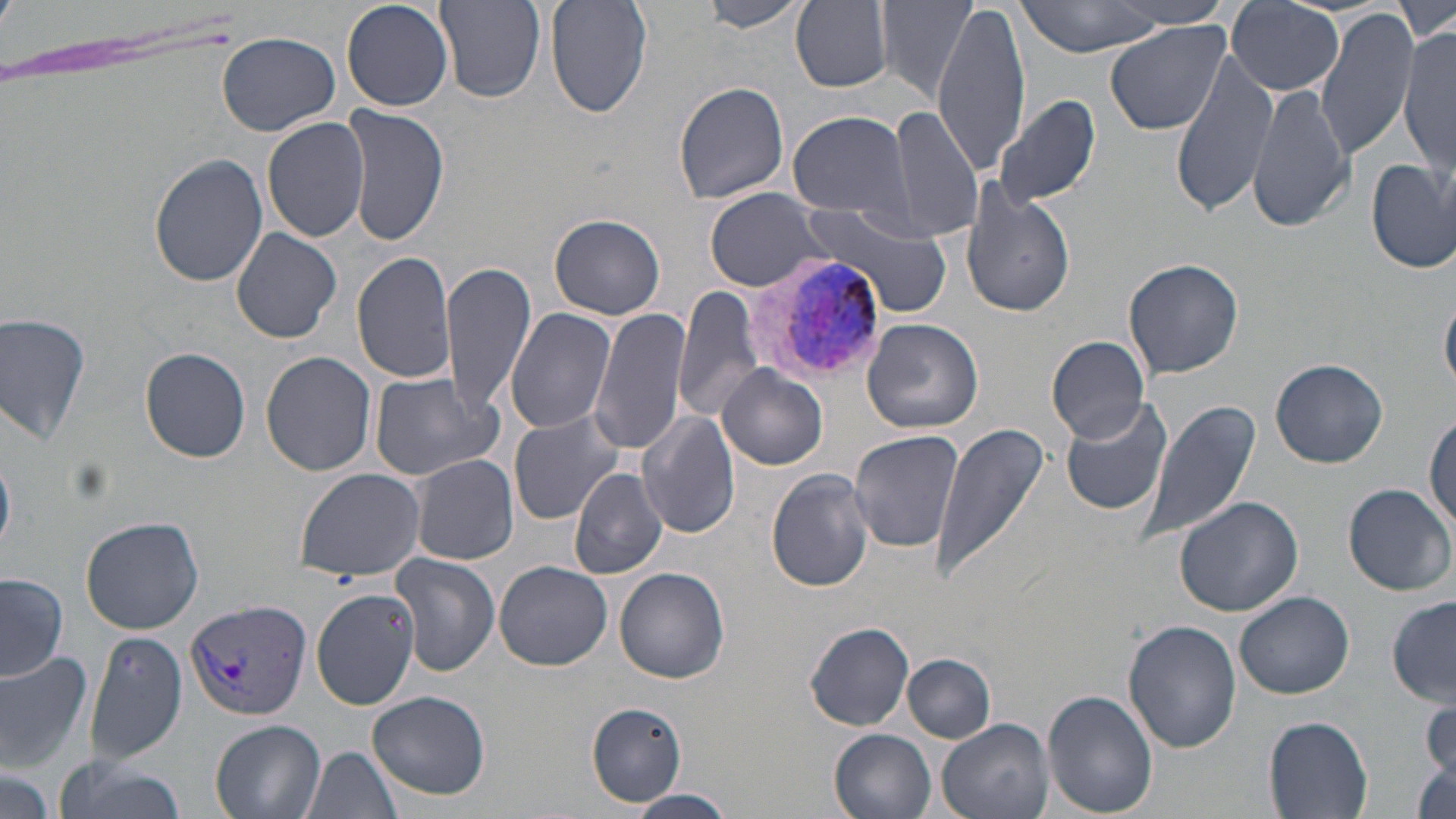

slide-level diagnosis = Plasmodium vivax
preparation = thin blood smear
field of view = one of a larger specimen
Plasmodium vivax-infected red blood cell locations = approximate bounding boxes as (x1,y1)-(x2,y2) corner pairs in pixels: (740,248)-(886,384), (183,597)-(311,723)
modality = light microscopy
magnification = 1000x
image size = 1456×819 pixels
uninfected red blood cell locations = approximate bounding boxes as (x1,y1)-(x2,y2) corner pairs in pixels: (342,0)-(454,112), (546,0)-(652,121), (875,0)-(978,101), (1012,0)-(1170,57), (1395,0)-(1455,44), (435,1)-(546,103), (701,1)-(809,33), (791,1)-(893,91), (1110,1)-(1234,30), (1224,2)-(1346,95), (931,5)-(1029,173), (1315,8)-(1417,162), (1104,19)-(1231,134), (1399,29)-(1455,169), (218,32)-(340,135), (1169,50)-(1278,219), (673,81)-(791,205), (1247,82)-(1354,234), (993,96)-(1102,210), (341,103)-(449,248), (885,105)-(983,241), (786,109)-(914,217), (261,116)-(370,243), (149,154)-(268,287), (1365,157)-(1455,274), (959,181)-(1077,319), (704,190)-(835,292), (806,202)-(955,321), (549,213)-(666,319), (230,227)-(342,343), (352,250)-(460,387), (1123,258)-(1244,380), (443,259)-(536,417), (673,286)-(764,425), (1441,292)-(1456,395), (593,307)-(690,457), (506,308)-(616,434), (0,313)-(92,447), (863,319)-(984,433), (1046,335)-(1150,444), (140,348)-(251,462), (260,351)-(375,476), (1271,358)-(1388,468), (718,366)-(828,469), (368,373)-(505,481), (1060,395)-(1177,515), (1138,399)-(1261,549), (636,408)-(740,540), (1428,408)-(1456,533), (508,410)-(627,523), (930,422)-(1052,586), (848,431)-(965,553), (411,455)-(518,564), (569,467)-(667,579), (295,468)-(424,582), (767,469)-(875,593), (1344,483)-(1454,596), (1174,495)-(1303,617), (81,516)-(204,633), (391,555)-(501,675), (494,560)-(612,670), (613,568)-(729,683), (0,574)-(68,680), (311,589)-(421,710), (1235,591)-(1354,699), (1387,596)-(1455,707), (1124,619)-(1242,754), (803,621)-(916,731), (84,632)-(187,763), (0,651)-(96,770), (904,655)-(996,742), (1041,688)-(1158,817), (368,689)-(491,801), (1421,698)-(1454,791), (587,703)-(687,805), (1262,714)-(1372,819), (934,717)-(1054,819), (209,719)-(326,819), (829,729)-(936,819), (302,744)-(405,819), (1411,754)-(1455,818), (50,759)-(186,819), (0,766)-(55,819), (629,790)-(736,816)
stain = May-Grünwald-Giemsa